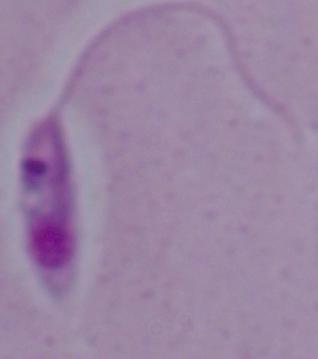

Micrograph. Captured at 1000x magnification. A Leishmania parasite is shown.